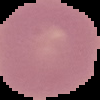 Malaria status: uninfected. From a thin blood smear. Cell region segmented out of the field of view; the surrounding area is masked to black. Image is 100×100 pixels.